Describe the morphology of the red blood cells.
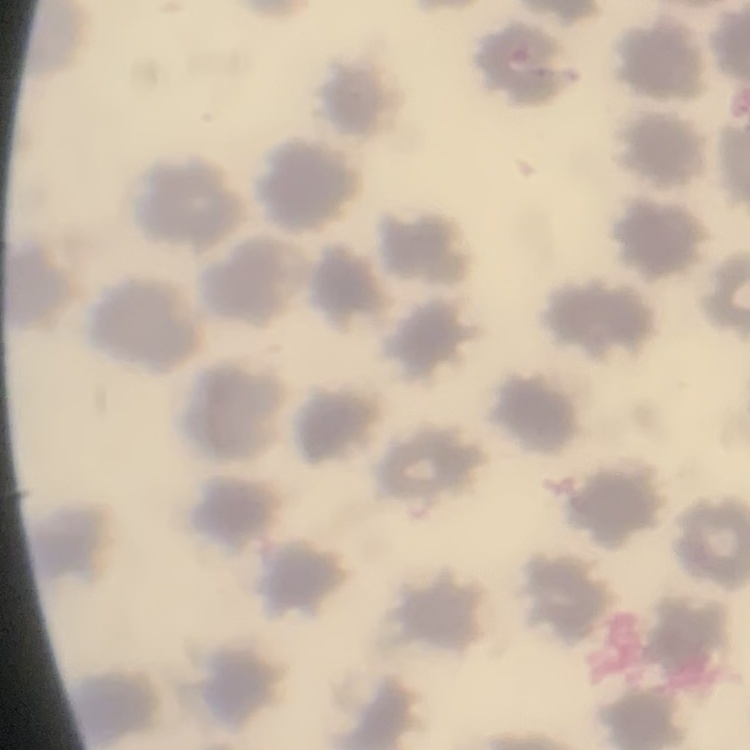

They show no rouleaux formation.

Summary:
  - Stain: Field's or Giemsa
  - Image type: one tile cut from a larger photomicrograph
  - Preparation: thin blood film